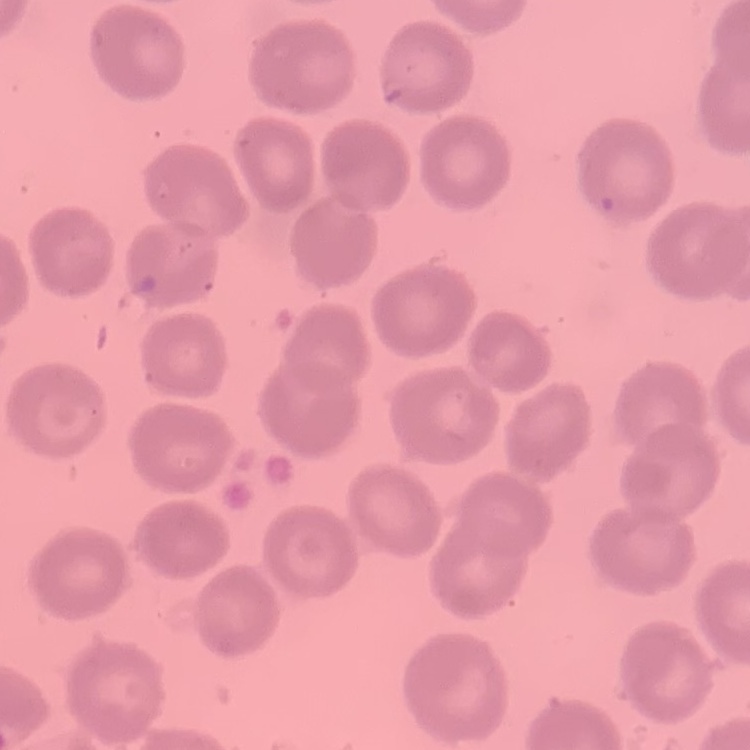
Summary:
  - Red blood cell morphology: no rouleaux formation
  - Image type: square crop of a larger photomicrograph
  - Preparation: thin blood smear
  - Stain: Field's or Giemsa